Classify this cell by malaria status.
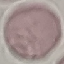

It is uninfected.

image type = cell patch, automatically extracted from a larger field of view and resized to 64 × 64 pixels
capture = smartphone through the microscope eyepiece
preparation = thin smear
stain = Giemsa